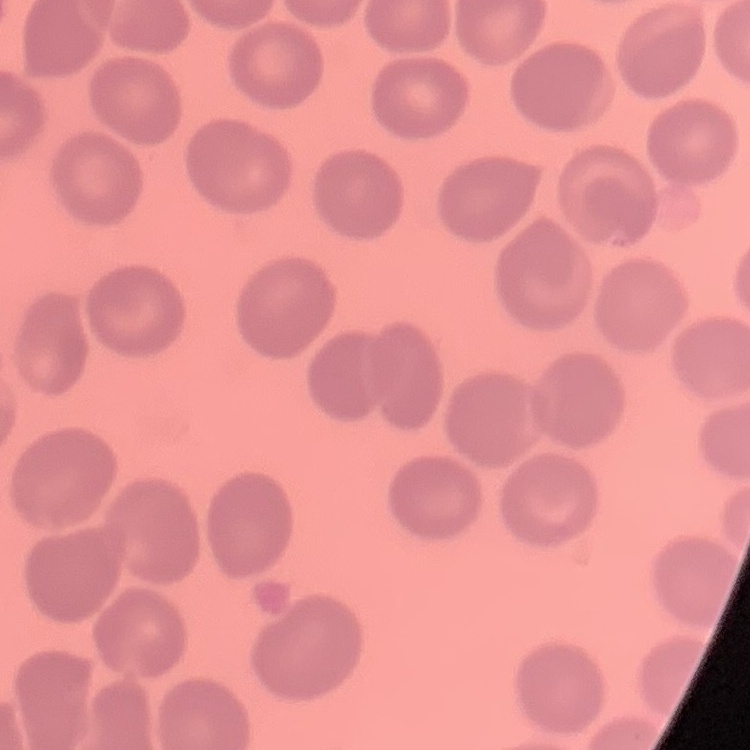

erythrocyte morphology = no rouleaux formation
preparation = thin peripheral smear
stain = Field's or Giemsa
image type = one tile cut from a larger photomicrograph